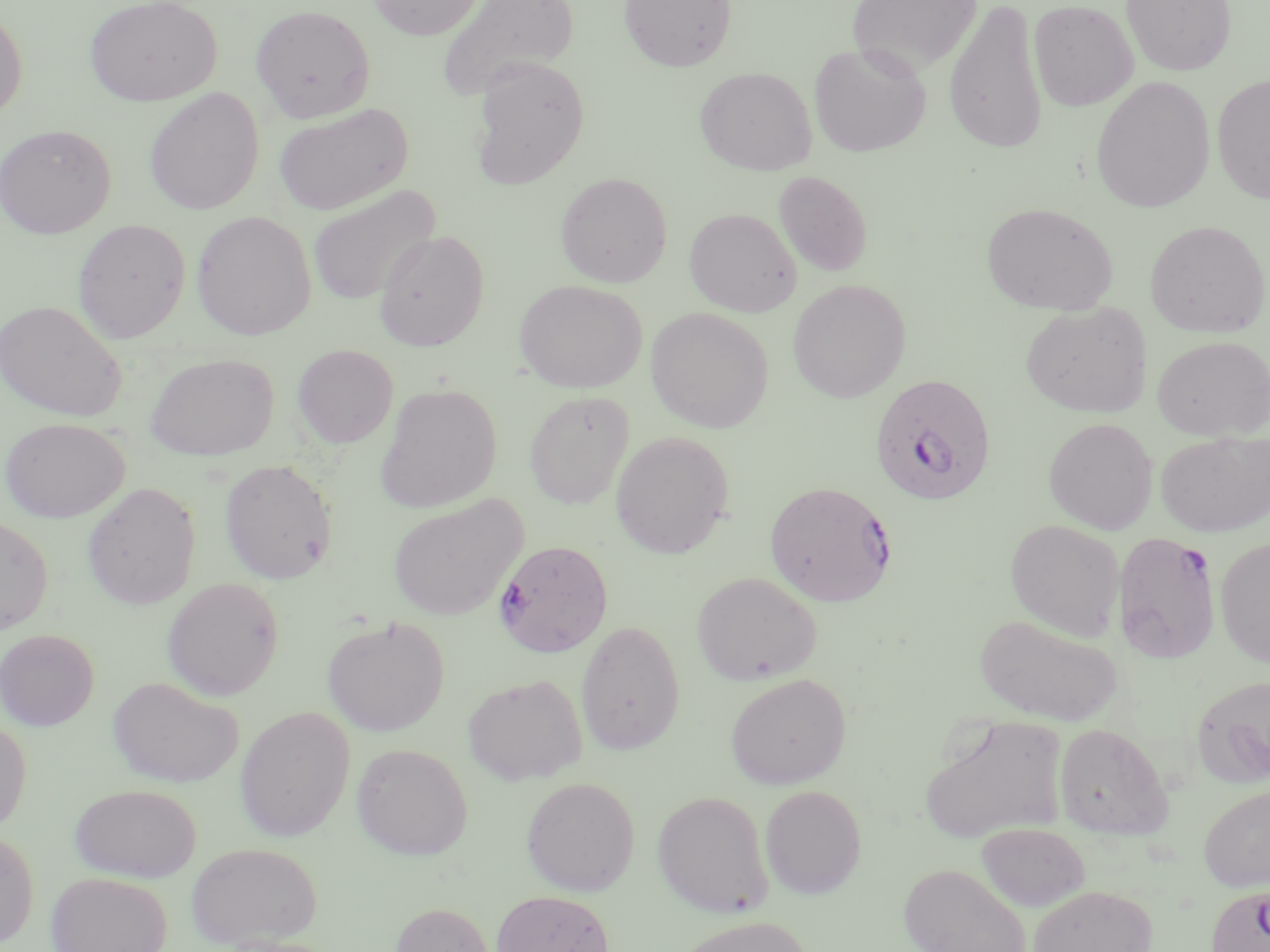

Approximate bounding boxes as (x1, y1, x2, y2) in pixels. Plasmodium falciparum-infected red blood cell locations: (869, 374, 997, 506), (764, 480, 897, 607), (1112, 532, 1221, 663), (494, 539, 613, 658), (1206, 884, 1270, 952). Uninfected red blood cell locations: (84, 0, 222, 106), (368, 0, 485, 40), (435, 0, 579, 101), (618, 0, 736, 72), (847, 0, 982, 77), (1028, 0, 1138, 111), (1121, 0, 1236, 76), (943, 1, 1048, 155), (250, 4, 375, 123), (0, 5, 28, 123), (809, 42, 932, 157), (469, 56, 590, 190), (695, 67, 816, 176), (1211, 73, 1270, 205), (1091, 76, 1215, 213), (144, 88, 264, 215), (273, 103, 412, 215), (0, 123, 116, 238), (773, 170, 873, 277), (555, 172, 672, 287), (308, 184, 441, 307), (981, 202, 1118, 316), (684, 208, 802, 317), (192, 211, 316, 340), (72, 219, 190, 343), (1145, 220, 1269, 337), (374, 230, 489, 351), (514, 279, 647, 393), (787, 279, 911, 403), (0, 299, 128, 422), (1020, 302, 1151, 418), (646, 307, 774, 432), (1152, 336, 1270, 440), (292, 344, 398, 449), (146, 352, 278, 461), (374, 383, 502, 513), (524, 391, 634, 510), (0, 417, 130, 523), (1043, 417, 1158, 534), (1155, 430, 1270, 537), (610, 431, 734, 559), (220, 459, 337, 584), (82, 482, 200, 610), (388, 495, 527, 620), (0, 515, 53, 635), (1005, 519, 1125, 640), (1215, 537, 1270, 668), (692, 571, 821, 685), (162, 577, 284, 701), (975, 613, 1124, 726), (322, 617, 449, 736), (575, 620, 686, 755), (0, 628, 100, 730), (462, 673, 588, 785), (725, 673, 851, 790), (1191, 673, 1270, 789), (108, 676, 244, 788), (235, 705, 355, 841), (921, 714, 1068, 845), (0, 717, 31, 835), (1053, 722, 1173, 840), (352, 742, 473, 860), (521, 776, 640, 896), (1198, 783, 1270, 891), (69, 784, 202, 882), (760, 784, 867, 899), (653, 790, 773, 918), (976, 822, 1090, 912), (0, 829, 39, 949), (186, 841, 323, 949), (899, 863, 1031, 952), (46, 871, 173, 952), (1028, 884, 1158, 952), (491, 889, 615, 952), (389, 901, 496, 952), (672, 915, 815, 952). Slide-level diagnosis: Plasmodium falciparum. May-Grünwald-Giemsa-stained preparation. 1000x magnification. Optical microscopy. Image is 1270×952 pixels. Thin blood smear. One field of a larger specimen.